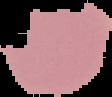

malaria status = uninfected
image size = 112×97 pixels
preparation = thin blood smear
image type = segmented cell region on a black background